Name the parasite shown.
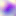

This is Toxoplasma gondii.

Photomicrograph. Captured at 400x magnification.